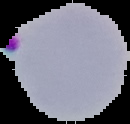

Summary:
  - Image type: segmented cell region on a black background
  - Preparation: thin blood film
  - Result: malaria parasites detected
  - Image size: 130×124 pixels